Give the position of every Plasmodium parasite.
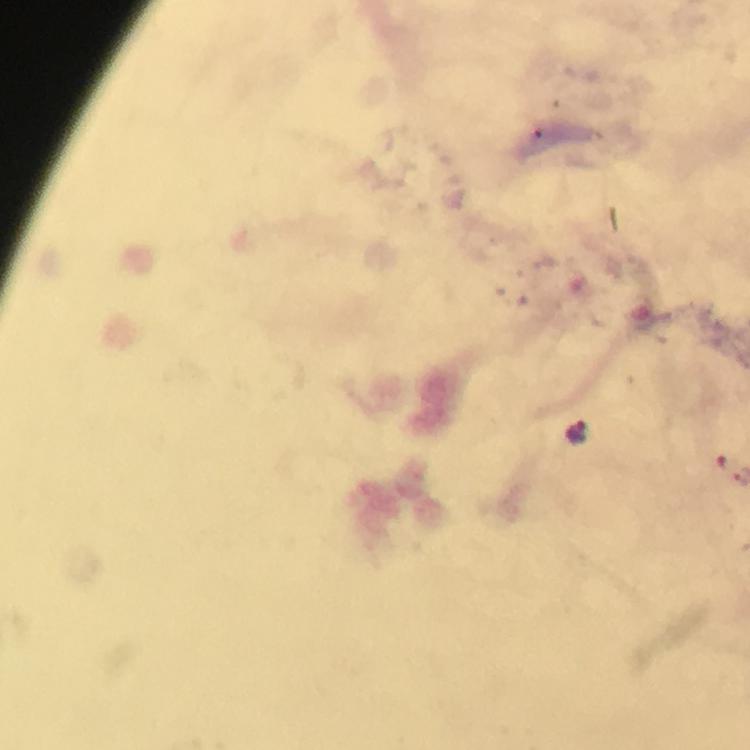
Approximate object centers, in pixels from the top-left corner.
Plasmodium parasites: (x=578, y=431).

Cropped region of a single field of view. At 100x magnification. Image is 750×750 pixels. Giemsa-stained preparation. Photographed through the microscope with a smartphone camera. From a malaria diagnostic workup. Thick blood smear. Immersion oil was used.